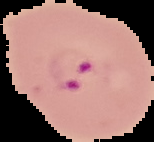

Image is 154×142 pixels. Result: Plasmodium parasites identified. The area outside the segmented cell region is set to black. From a thin blood smear.